Give the position of every Plasmodium parasite.
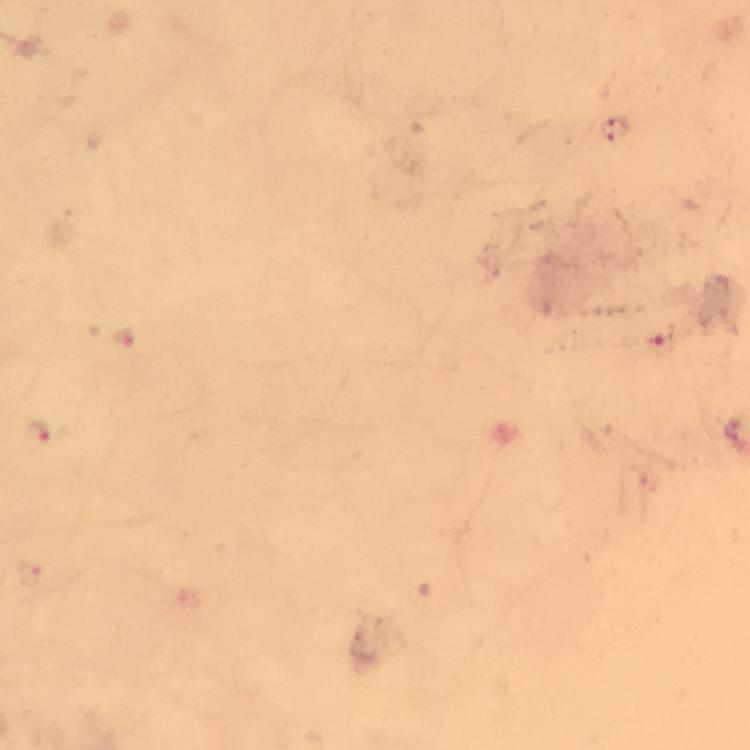
Approximate centers as [x, y] in pixels.
Plasmodium parasites: [614, 131], [124, 337], [659, 345], [37, 432].

Photographed through the microscope with a smartphone camera. Giemsa stain. Image is 750×750 pixels. Immersion oil applied. From a diagnostic examination for malaria. A crop from one field of view. At 100x magnification. Thick blood smear.